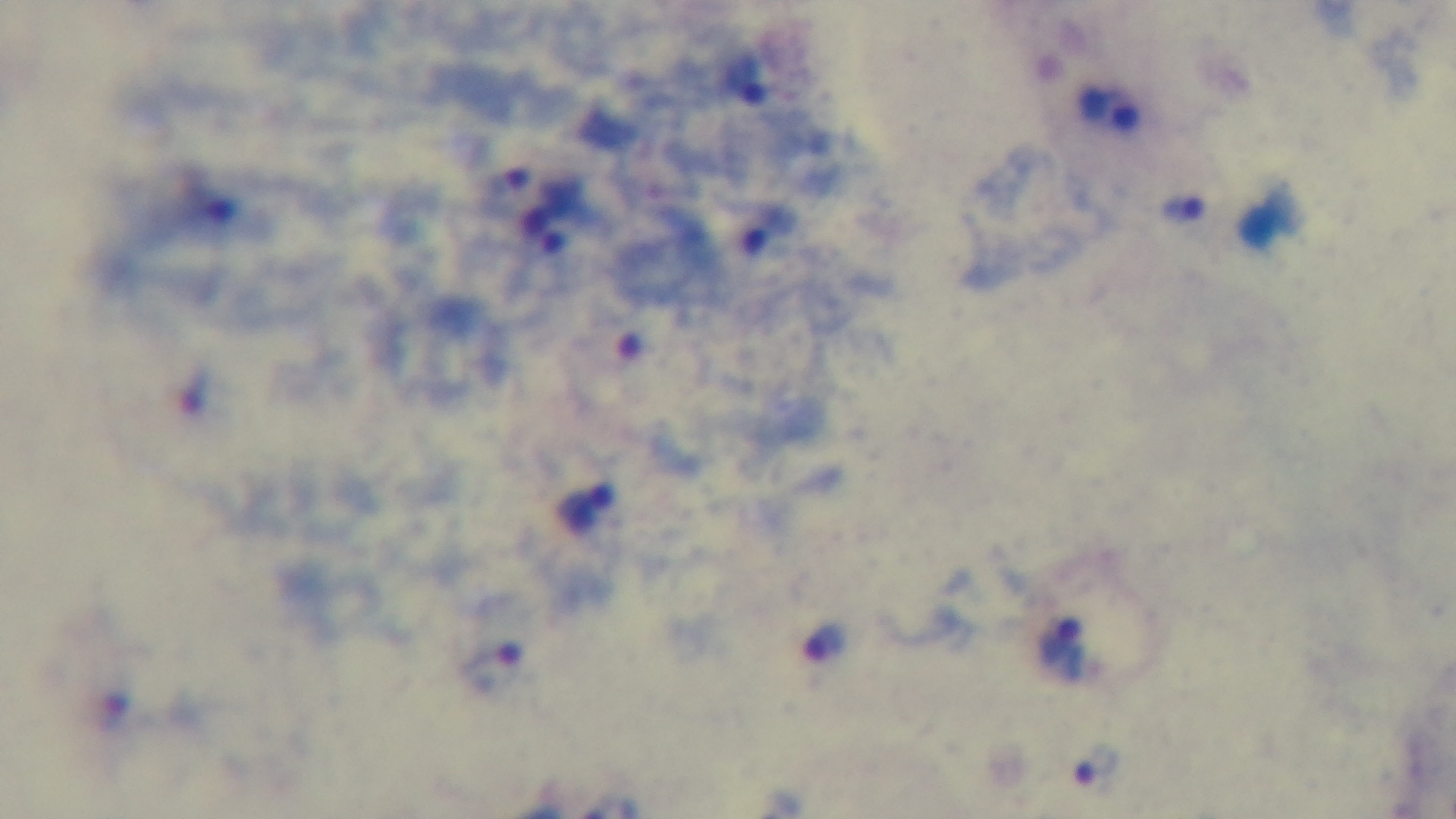 100x oil-immersion objective. Giemsa stain. Preparation: thick. Captured with a mounted 4K digital camera. Single field of view. Photomicrograph. Malaria status: infected.